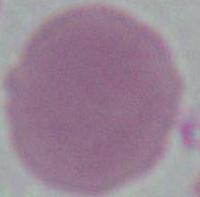
Summary:
  - Modality: photomicrograph
  - Identification: erythrocyte
  - Magnification: 1000x